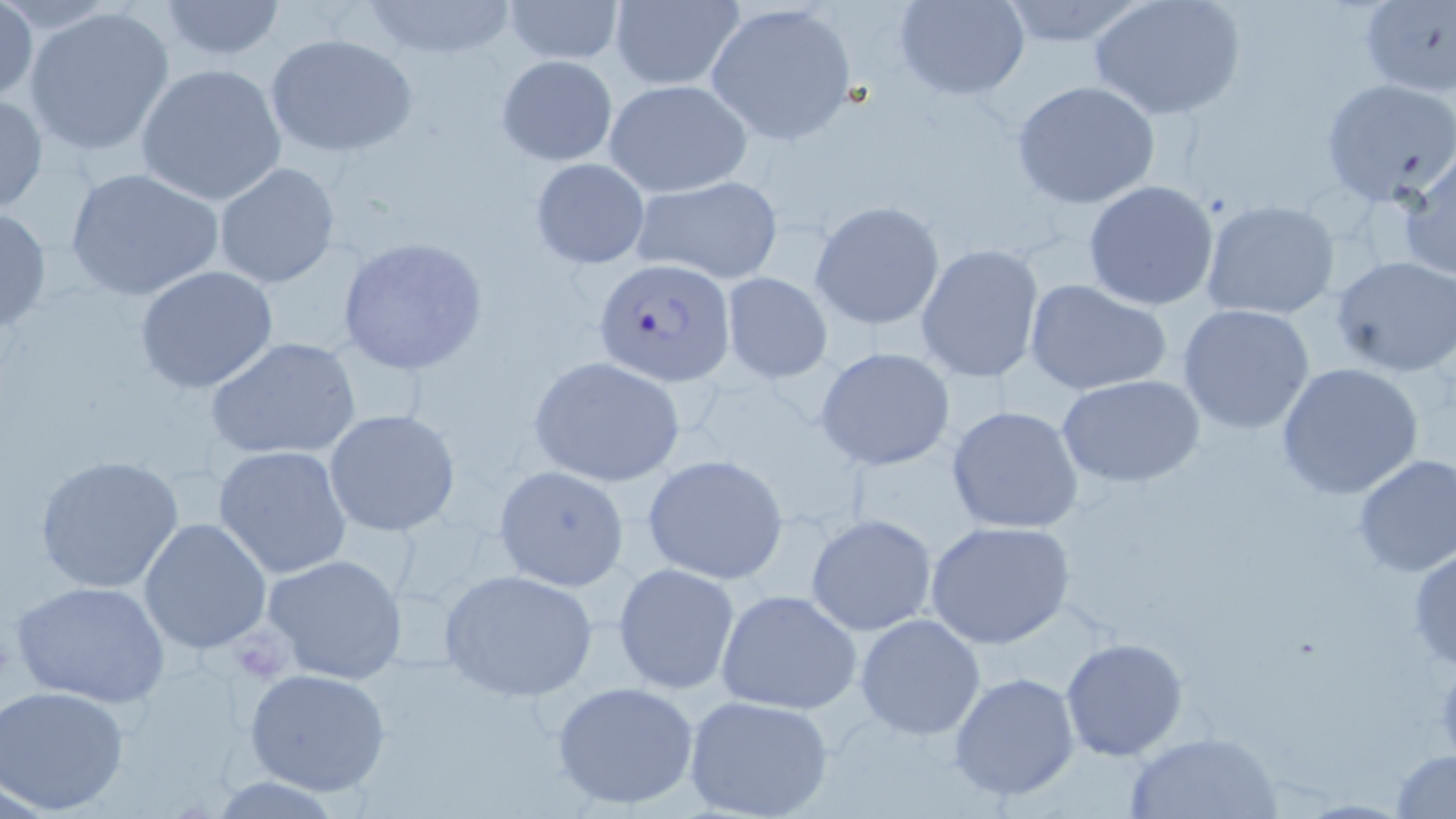

Approximate bounding boxes as (x1, y1, x2, y2) in pixels. Uninfected red blood cell locations: (503, 0, 623, 65), (608, 0, 745, 90), (895, 0, 1030, 101), (996, 0, 1149, 48), (1088, 0, 1247, 121), (1359, 0, 1454, 97), (157, 1, 286, 60), (360, 1, 519, 61), (705, 2, 858, 145), (0, 3, 37, 106), (23, 4, 176, 159), (264, 33, 417, 158), (496, 54, 618, 166), (135, 62, 287, 205), (1320, 79, 1456, 208), (605, 80, 752, 198), (1011, 80, 1162, 210), (0, 91, 48, 216), (1398, 153, 1456, 281), (529, 157, 651, 269), (213, 163, 341, 288), (63, 165, 230, 305), (631, 175, 784, 284), (1083, 181, 1220, 311), (1200, 199, 1342, 321), (810, 200, 945, 330), (0, 207, 51, 336), (336, 237, 489, 375), (915, 243, 1045, 384), (1331, 255, 1456, 375), (134, 264, 279, 394), (719, 271, 834, 383), (1024, 278, 1174, 398), (1176, 302, 1318, 435), (207, 337, 361, 463), (814, 346, 956, 471), (527, 355, 685, 488), (1274, 362, 1426, 500), (1060, 374, 1206, 488), (946, 405, 1087, 535), (323, 409, 461, 537), (213, 445, 352, 578), (33, 453, 189, 596), (642, 454, 790, 585), (1351, 455, 1456, 578), (492, 464, 630, 591), (806, 514, 937, 637), (138, 517, 274, 654), (925, 520, 1075, 650), (1407, 541, 1456, 670), (262, 554, 408, 684), (613, 562, 741, 695), (439, 567, 598, 701), (10, 580, 171, 708), (715, 589, 864, 715), (854, 612, 986, 740), (1059, 636, 1188, 760), (243, 667, 391, 796), (949, 671, 1080, 803), (550, 679, 702, 810), (1, 686, 130, 813), (683, 695, 834, 819), (1126, 731, 1281, 817), (1389, 749, 1456, 819). Platelet locations: (1431, 659, 1456, 757). Plasmodium falciparum-infected red blood cell locations: (594, 258, 738, 386). Slide-level diagnosis: Plasmodium falciparum. Image is 1456×819 pixels. Captured at 1000x magnification. May-Grünwald-Giemsa-stained preparation. Single field of view. Thin blood smear. Optical microscopy.